Give the position of each Plasmodium falciparum parasite with its life-cycle stage, each leukocyte, and any debris.
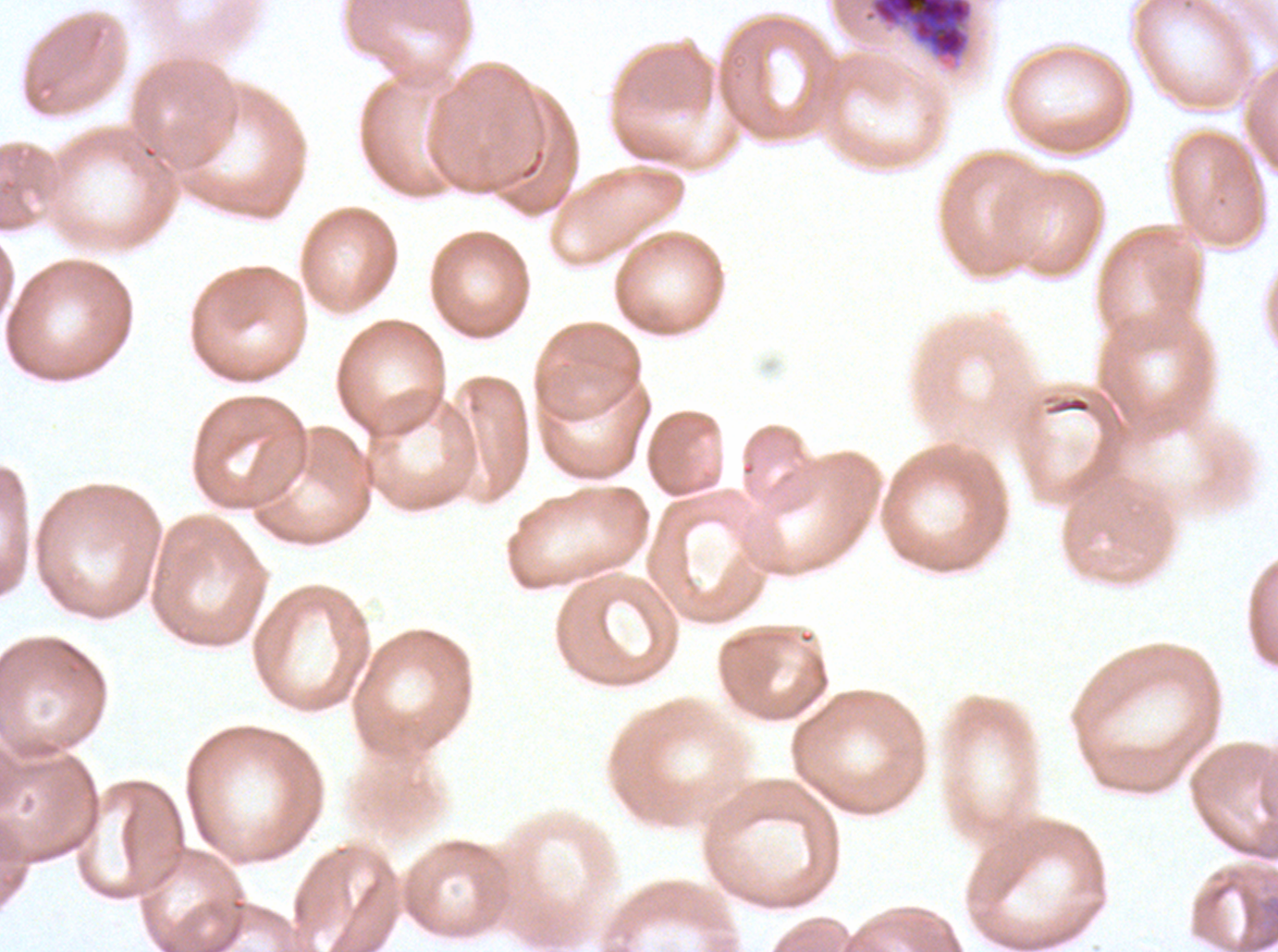

Approximate bounding boxes as (x1, y1, x2, y2) in pixels.
Early schizonts: (865, 0, 974, 61).
No rings, late-ring/early-trophozoite forms, mid trophozoites, late trophozoites, late schizonts, segmenters, gametocytes, leukocytes, or debris observed.

Thin blood smear. Plasmodium falciparum from a patient in The Gambia, cultured ex vivo for 24 to 48 hours. Giemsa stain. Image is 1278×952 pixels. One sub-image of a larger composite.